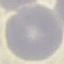
malaria status = uninfected
image type = automatically extracted cell patch, resized to 64 × 64 pixels
capture = smartphone through the microscope eyepiece
preparation = thin smear
stain = Giemsa